Outline each Plasmodium vivax-infected red blood cell.
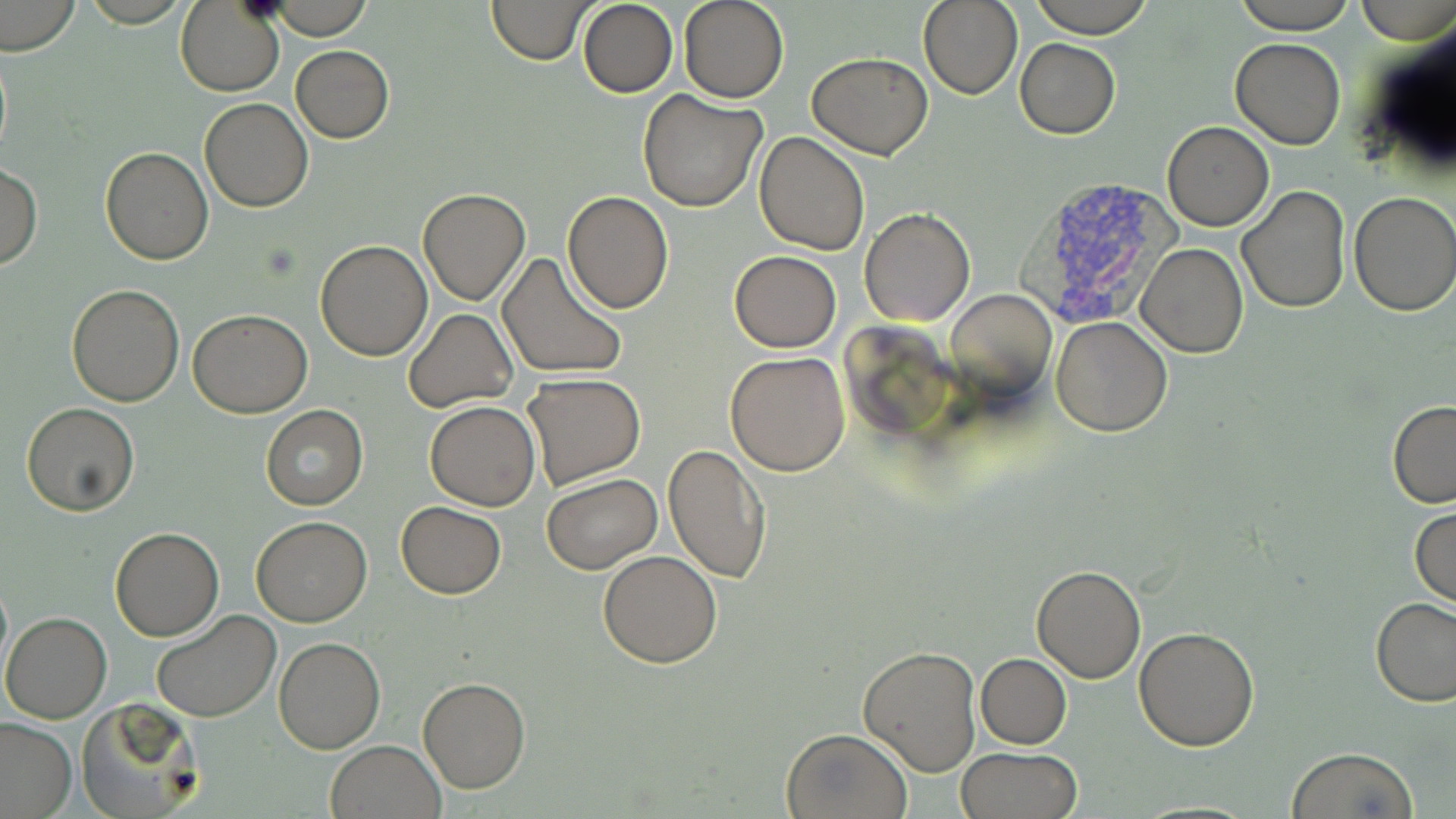
Approximate bounding boxes as named x1/y1/x2/y2 corners in pixels.
Plasmodium vivax-infected red blood cells: (x1=1011, y1=174, x2=1181, y2=330).

slide-level diagnosis = Plasmodium vivax
modality = light microscopy
stain = May-Grünwald-Giemsa
uninfected red blood cell locations = approximate bounding boxes as named x1/y1/x2/y2 corners in pixels: (x1=1, y1=0, x2=81, y2=58), (x1=487, y1=0, x2=595, y2=65), (x1=679, y1=0, x2=789, y2=103), (x1=918, y1=0, x2=1023, y2=101), (x1=1027, y1=0, x2=1157, y2=37), (x1=1234, y1=0, x2=1358, y2=33), (x1=1358, y1=0, x2=1455, y2=44), (x1=577, y1=1, x2=678, y2=98), (x1=176, y1=2, x2=285, y2=97), (x1=260, y1=2, x2=381, y2=37), (x1=1357, y1=12, x2=1456, y2=183), (x1=1231, y1=37, x2=1345, y2=149), (x1=1015, y1=38, x2=1120, y2=138), (x1=290, y1=46, x2=393, y2=143), (x1=807, y1=51, x2=933, y2=158), (x1=637, y1=88, x2=768, y2=212), (x1=199, y1=98, x2=313, y2=212), (x1=1162, y1=121, x2=1274, y2=232), (x1=753, y1=132, x2=871, y2=257), (x1=100, y1=146, x2=213, y2=264), (x1=1, y1=162, x2=41, y2=271), (x1=1236, y1=185, x2=1352, y2=314), (x1=418, y1=188, x2=531, y2=305), (x1=563, y1=190, x2=674, y2=313), (x1=1349, y1=192, x2=1456, y2=317), (x1=860, y1=209, x2=975, y2=328), (x1=315, y1=239, x2=432, y2=360), (x1=1136, y1=243, x2=1248, y2=359), (x1=729, y1=250, x2=842, y2=352), (x1=498, y1=251, x2=629, y2=382), (x1=66, y1=283, x2=184, y2=406), (x1=945, y1=289, x2=1058, y2=404), (x1=188, y1=309, x2=311, y2=417), (x1=404, y1=309, x2=518, y2=414), (x1=1052, y1=316, x2=1173, y2=437), (x1=725, y1=352, x2=850, y2=476), (x1=521, y1=373, x2=649, y2=494), (x1=424, y1=400, x2=540, y2=511), (x1=1386, y1=400, x2=1456, y2=509), (x1=21, y1=403, x2=140, y2=515), (x1=261, y1=405, x2=368, y2=511), (x1=662, y1=442, x2=772, y2=585), (x1=542, y1=474, x2=662, y2=574), (x1=395, y1=501, x2=506, y2=599), (x1=1410, y1=506, x2=1455, y2=610), (x1=251, y1=515, x2=372, y2=627), (x1=110, y1=528, x2=225, y2=642), (x1=598, y1=550, x2=722, y2=668), (x1=1031, y1=564, x2=1146, y2=682), (x1=0, y1=574, x2=12, y2=682), (x1=1372, y1=599, x2=1456, y2=705), (x1=150, y1=610, x2=280, y2=723), (x1=2, y1=612, x2=112, y2=723), (x1=1133, y1=626, x2=1260, y2=751), (x1=274, y1=638, x2=386, y2=754), (x1=858, y1=645, x2=982, y2=774), (x1=976, y1=652, x2=1072, y2=749), (x1=417, y1=677, x2=531, y2=795), (x1=74, y1=696, x2=203, y2=818), (x1=0, y1=718, x2=76, y2=817), (x1=782, y1=727, x2=913, y2=819), (x1=325, y1=740, x2=446, y2=818), (x1=1285, y1=747, x2=1420, y2=819), (x1=954, y1=748, x2=1081, y2=819)
magnification = 1000x
image size = 1456×819 pixels
preparation = thin blood smear
field of view = single